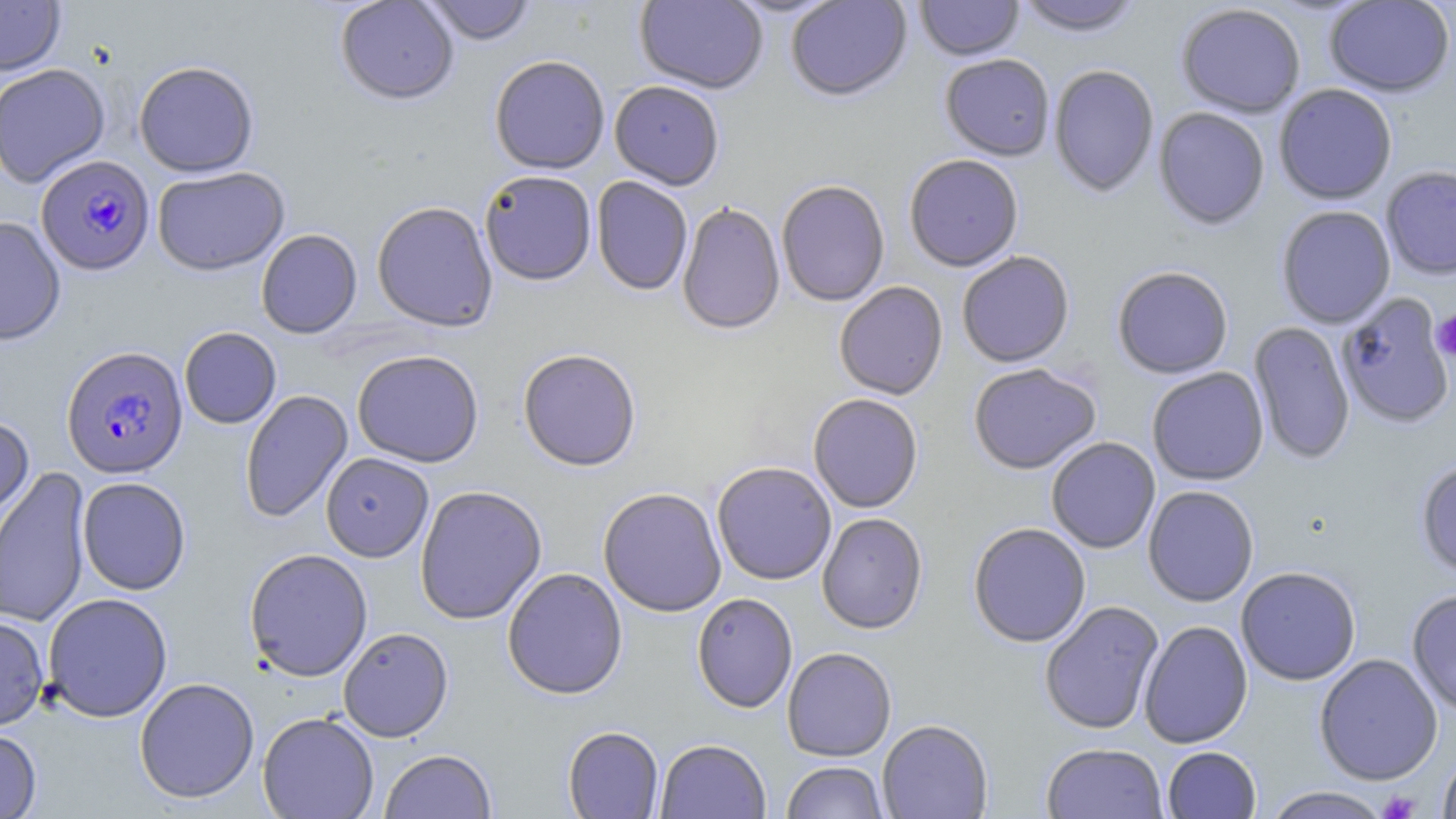

slide-level diagnosis = Plasmodium falciparum
modality = light microscopy
magnification = 1000x
uninfected red blood cell locations = approximate bounding boxes as (x1, y1, x2, y2) in pixels: (335, 0, 459, 105), (421, 0, 536, 46), (635, 0, 768, 95), (786, 0, 912, 103), (915, 0, 1024, 62), (1014, 0, 1145, 39), (0, 1, 66, 77), (1324, 1, 1455, 98), (1175, 4, 1305, 119), (940, 55, 1055, 162), (490, 56, 610, 175), (133, 60, 259, 177), (0, 64, 111, 187), (1048, 66, 1159, 199), (609, 81, 724, 191), (1274, 85, 1398, 205), (1153, 108, 1270, 232), (904, 156, 1024, 272), (1381, 166, 1456, 281), (152, 167, 290, 276), (479, 170, 596, 286), (591, 177, 692, 296), (776, 181, 890, 307), (372, 202, 498, 332), (677, 203, 785, 336), (1276, 206, 1396, 329), (0, 216, 66, 345), (256, 229, 362, 339), (957, 252, 1075, 368), (1112, 267, 1233, 380), (834, 282, 948, 401), (1337, 293, 1453, 428), (1249, 321, 1355, 466), (179, 327, 282, 429), (351, 349, 484, 467), (518, 350, 641, 472), (968, 364, 1101, 475), (1147, 367, 1269, 486), (240, 390, 353, 523), (808, 394, 923, 514), (0, 415, 35, 538), (1046, 438, 1160, 554), (321, 452, 434, 563), (1415, 460, 1456, 581), (712, 462, 836, 586), (0, 468, 92, 628), (77, 477, 191, 595), (415, 485, 547, 625), (1143, 486, 1259, 607), (598, 487, 727, 617), (817, 513, 928, 634), (968, 523, 1091, 647), (244, 548, 373, 681), (1235, 566, 1361, 686), (502, 568, 628, 700), (1407, 589, 1456, 716), (42, 592, 173, 722), (692, 593, 797, 714), (1039, 601, 1164, 735), (0, 614, 49, 730), (1138, 621, 1253, 749), (338, 627, 454, 742), (782, 647, 897, 762), (1314, 653, 1443, 785), (134, 677, 259, 804), (257, 711, 379, 818), (877, 719, 993, 819), (563, 726, 664, 819), (0, 728, 41, 818), (656, 739, 771, 819), (1041, 743, 1168, 818), (1162, 746, 1261, 818), (379, 749, 497, 819), (1437, 750, 1456, 819), (781, 761, 890, 819), (1263, 786, 1392, 818)
field of view = single
stain = May-Grünwald-Giemsa
platelet locations = approximate bounding boxes as (x1, y1, x2, y2) in pixels: (1431, 311, 1456, 362), (1378, 790, 1421, 818)
image size = 1456×819 pixels
Plasmodium falciparum-infected red blood cell locations = approximate bounding boxes as (x1, y1, x2, y2) in pixels: (36, 155, 155, 276), (61, 345, 189, 479)
preparation = thin blood smear